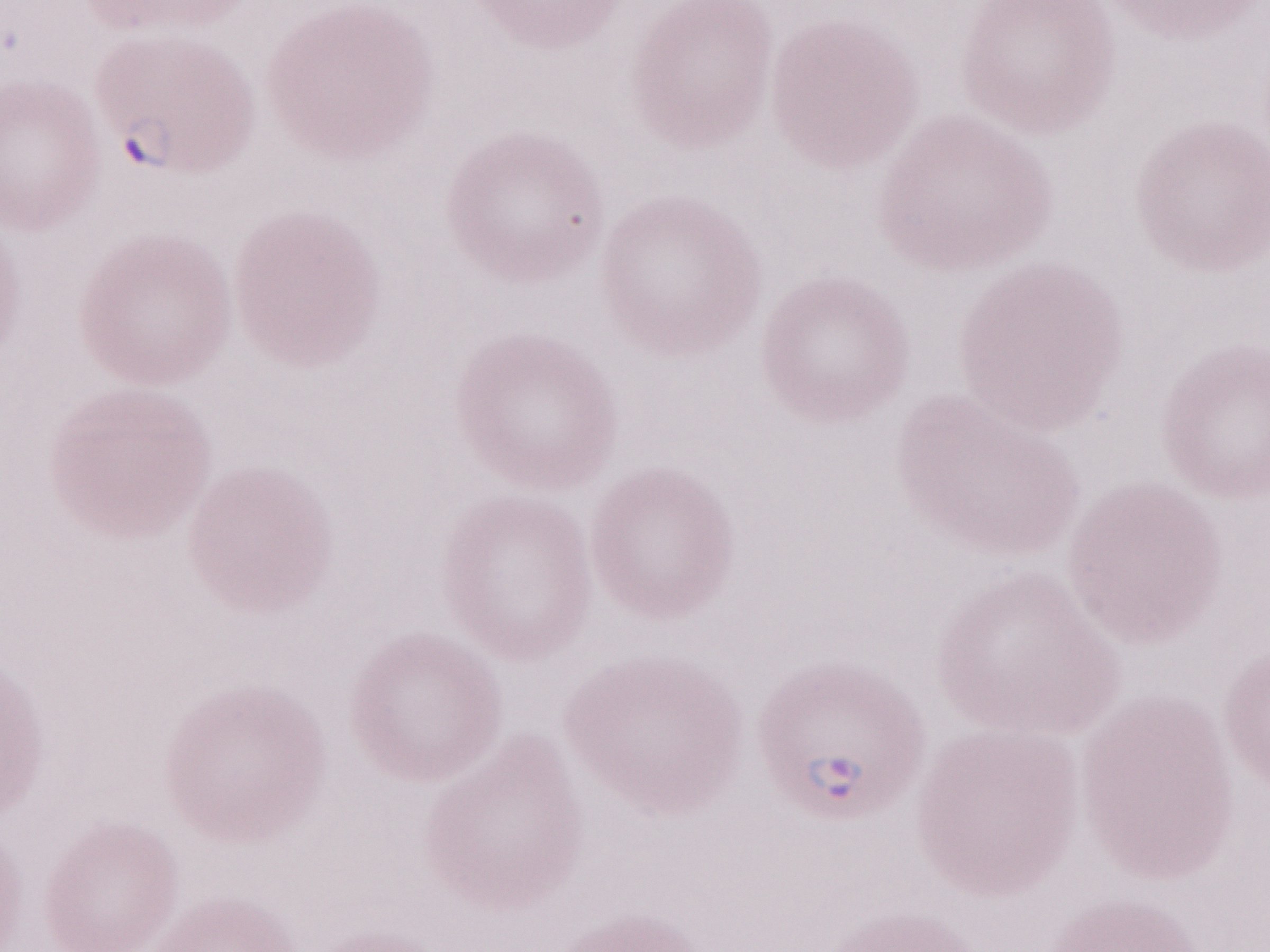
Olympus BX43 microscope, Olympus DP73 camera. Thin blood smear. Patient diagnosis: malaria infection. Single field of view. May-Grünwald-Giemsa stain. 1,000x magnification. Image is 1270×952 pixels.